Assess this cell for malaria.
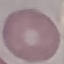

Uninfected.

Giemsa stain. Photographed with a smartphone camera at the microscope eyepiece. Automatically extracted cell patch, resized to 64 × 64 pixels. Thin blood film.